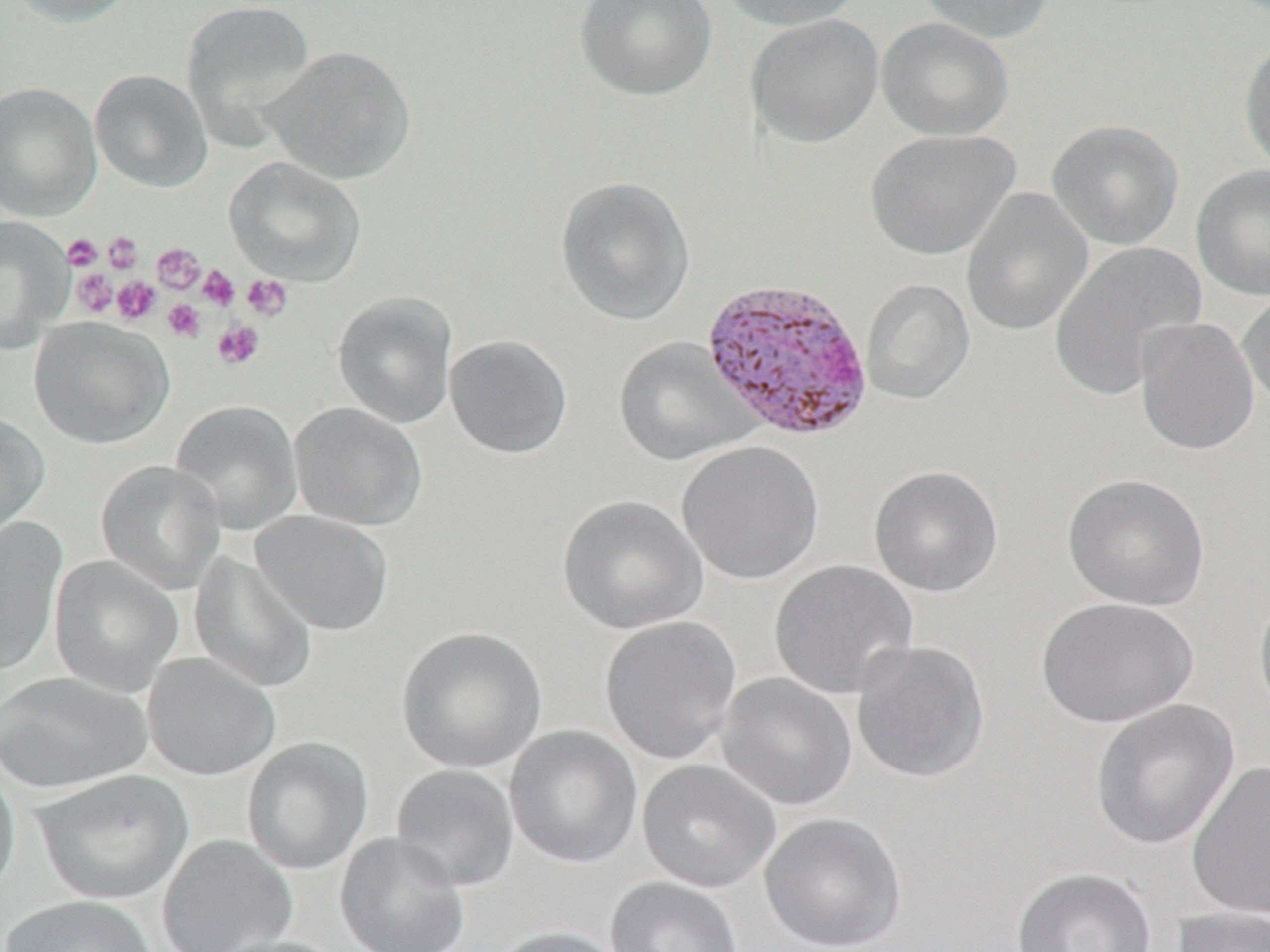
Summary:
  - Coordinate format: approximate bounding boxes as (x1,y1)-(x2,y2) corner pairs in pixels
  - Platelet locations: (103,231)-(143,274), (62,234)-(102,270), (152,242)-(204,293), (198,265)-(239,310), (72,269)-(118,317), (241,274)-(294,321), (112,276)-(160,325), (162,299)-(205,343), (213,320)-(265,370)
  - Plasmodium vivax-infected red blood cell locations: (699,276)-(874,442)
  - Uninfected red blood cell locations: (3,0)-(138,27), (179,0)-(317,149), (575,0)-(717,102), (715,0)-(864,31), (916,0)-(1056,44), (745,13)-(884,148), (877,16)-(1014,142), (1238,37)-(1270,175), (262,44)-(416,185), (90,68)-(213,193), (0,80)-(102,222), (1047,119)-(1184,251), (865,129)-(1018,261), (224,156)-(367,286), (1191,164)-(1270,301), (555,175)-(695,325), (961,187)-(1093,337), (0,216)-(73,355), (1048,241)-(1207,402), (860,278)-(975,405), (1237,288)-(1270,412), (332,291)-(458,429), (28,316)-(174,449), (1134,316)-(1260,457), (445,334)-(573,459), (613,337)-(757,466), (170,400)-(303,534), (289,402)-(427,532), (0,411)-(50,545), (677,440)-(825,585), (96,460)-(226,593), (869,465)-(1004,598), (1063,473)-(1210,611), (557,494)-(709,635), (251,510)-(394,636), (0,517)-(67,677), (189,551)-(318,694), (50,555)-(183,696), (768,560)-(919,700), (1253,586)-(1270,721), (1035,596)-(1198,728), (600,615)-(743,765), (396,626)-(547,774), (851,639)-(991,784), (142,653)-(281,781), (0,671)-(151,794), (716,672)-(858,811), (1090,699)-(1239,851), (504,725)-(643,869), (242,737)-(373,875), (0,758)-(21,905), (637,759)-(781,893), (1187,759)-(1270,922), (390,764)-(520,892), (32,769)-(194,905), (759,812)-(907,952), (335,831)-(471,952), (157,834)-(298,952), (1011,866)-(1158,952), (605,877)-(744,952), (1,895)-(158,952), (1170,906)-(1270,952), (492,925)-(630,952), (208,935)-(349,952)
  - Slide-level diagnosis: Plasmodium vivax
  - Magnification: 1000x
  - Preparation: thin blood smear
  - Image size: 1270×952 pixels
  - Field of view: one of a larger specimen
  - Stain: May-Grünwald-Giemsa
  - Modality: light microscopy